Give the position of every malaria parasite.
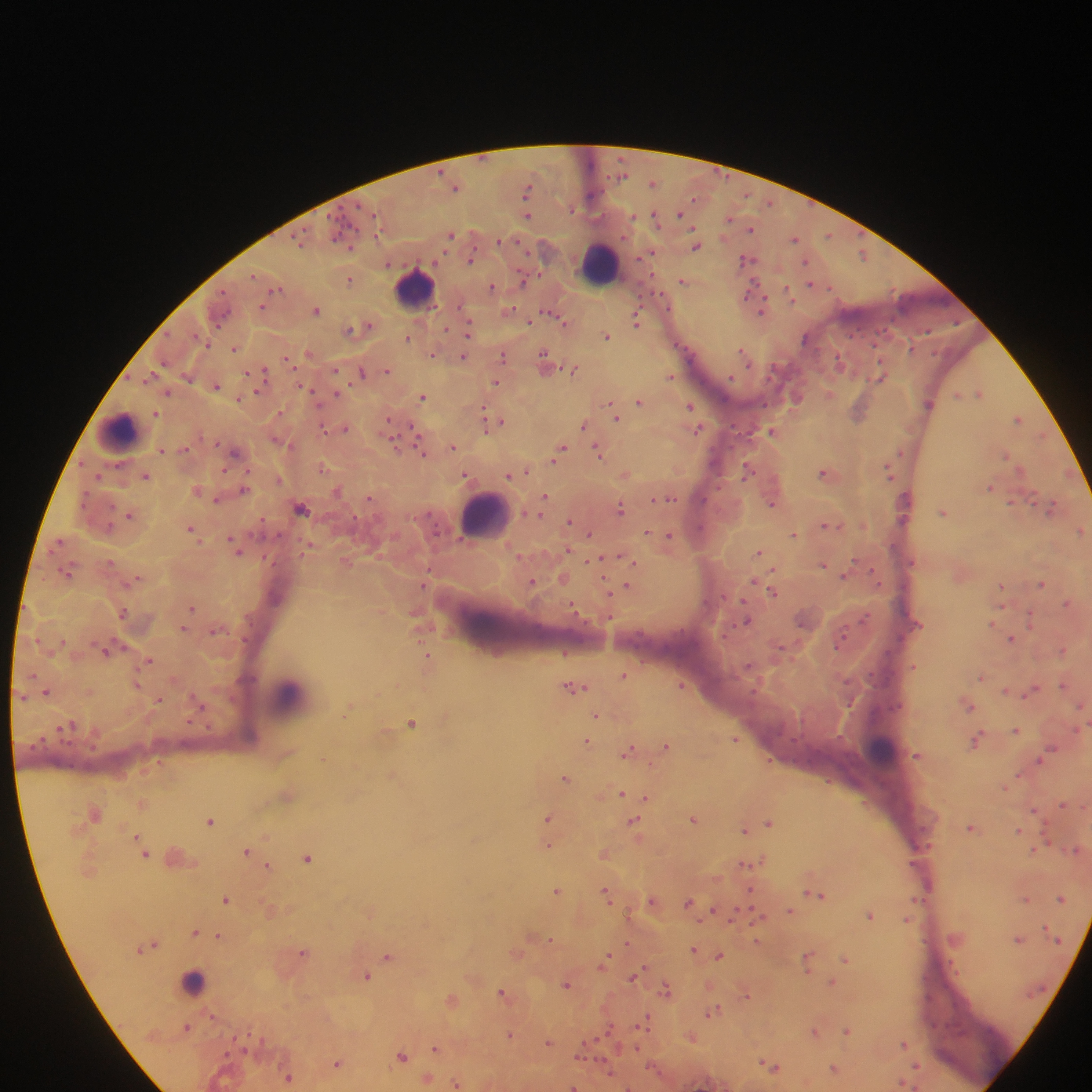
Approximate centers as [x, y] in pixels.
Malaria parasites: [652, 182], [455, 186], [527, 190], [680, 214], [527, 216], [656, 217], [730, 218], [752, 229], [451, 235], [829, 235], [795, 238], [696, 245], [652, 252], [863, 254], [471, 259], [747, 259], [806, 261], [350, 279], [683, 280], [812, 284], [492, 287], [751, 294], [790, 295], [263, 306], [761, 306], [316, 309], [510, 310], [553, 312], [636, 319], [560, 320], [530, 321], [364, 327], [469, 328], [351, 330], [408, 336], [607, 336], [235, 349], [743, 351], [309, 353], [432, 354], [503, 355], [463, 357], [288, 360], [545, 360], [840, 361], [336, 369], [574, 369], [388, 370], [361, 372], [261, 373], [881, 375], [671, 377], [496, 381], [217, 386], [168, 392], [980, 392], [337, 394], [830, 394], [959, 394], [423, 396], [796, 397], [240, 398], [640, 401], [929, 403], [691, 406], [859, 411], [156, 413], [615, 416], [1019, 418], [494, 421], [501, 421], [584, 425], [344, 429], [697, 429], [772, 430], [417, 434], [1042, 434], [419, 443], [395, 445], [453, 447], [161, 450], [599, 450], [236, 452], [560, 452], [1006, 454], [323, 468], [749, 468], [890, 470], [522, 471], [826, 473], [511, 474], [625, 474], [146, 476], [467, 476], [991, 487], [245, 489], [199, 490], [337, 490], [545, 497], [369, 498], [656, 498], [669, 498], [218, 499], [773, 503], [542, 506], [621, 507], [301, 508], [1051, 508], [943, 511], [130, 515], [570, 521], [828, 525], [191, 528], [1080, 529], [648, 532], [589, 534], [794, 534], [670, 536], [60, 541], [237, 548], [568, 549], [760, 551], [622, 557], [607, 558], [599, 561], [345, 562], [823, 565], [67, 572], [846, 574], [563, 578], [136, 580], [755, 581], [533, 582], [1042, 582], [425, 583], [627, 586], [1002, 586], [774, 591], [1068, 602], [571, 606], [192, 607], [124, 612], [1031, 619], [748, 620], [992, 623], [184, 628], [1012, 639], [108, 649], [1063, 650], [565, 652], [428, 659], [149, 661], [914, 666], [624, 675], [982, 676], [137, 683], [1064, 684], [682, 685], [575, 688], [1006, 691], [1031, 691], [47, 692], [159, 699], [1082, 704], [968, 705], [349, 708], [597, 715], [412, 722], [64, 727], [1016, 730], [735, 738], [978, 739], [587, 741], [667, 745], [629, 750], [917, 754], [1040, 760], [393, 775], [1019, 775], [566, 777], [622, 793], [288, 794], [635, 795], [647, 798], [142, 803], [1062, 804], [1034, 809], [95, 813], [549, 817], [694, 819], [210, 820], [769, 822], [635, 823], [755, 827], [972, 827], [745, 829], [1018, 829], [138, 836], [548, 844], [1034, 849], [248, 850], [604, 852], [145, 853], [308, 856], [747, 864], [269, 865], [557, 890], [751, 890], [607, 893], [815, 894], [226, 898], [1026, 898], [1061, 899], [653, 901], [690, 903], [270, 909], [715, 910], [791, 911], [372, 912], [871, 914], [757, 915], [907, 919], [195, 931], [218, 936], [543, 937], [551, 938], [1019, 939], [757, 941], [151, 944], [628, 944], [694, 950], [304, 951], [517, 952], [720, 955], [388, 956], [845, 958], [809, 959], [606, 960], [367, 975], [635, 976], [831, 982], [567, 984], [667, 989], [504, 993], [746, 994], [453, 1000], [713, 1011], [213, 1016], [645, 1021], [187, 1027], [847, 1030], [815, 1031], [510, 1034], [692, 1037], [548, 1042], [904, 1043], [436, 1047], [636, 1048], [402, 1056], [338, 1063], [771, 1065], [916, 1067], [835, 1069], [609, 1071], [289, 1076], [428, 1078], [457, 1082], [905, 1083], [573, 1086].

preparation = thick blood film
field of view = single
image size = 1092×1092 pixels
capture = mobile-phone photograph through a microscope
leukocyte locations = approximate centers as [x, y] in pixels: [600, 264], [415, 289], [117, 431], [486, 515], [289, 699], [881, 749], [179, 857], [194, 981], [970, 1014]
country = Ghana